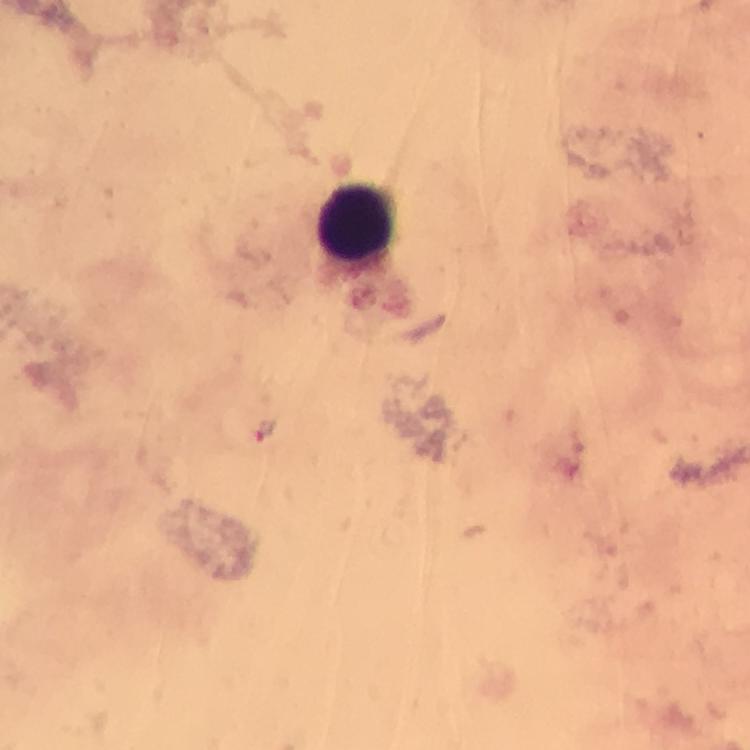
Approximate centers as [x, y] in pixels. Leukocyte locations: [359, 223]. Plasmodium parasite locations: [265, 429]. Giemsa-stained preparation. Photographed with a smartphone mounted on the microscope. At 100x magnification. Image is 750×750 pixels. Thick smear. From a diagnostic examination for malaria. A crop from one field of view. Immersion oil was used.